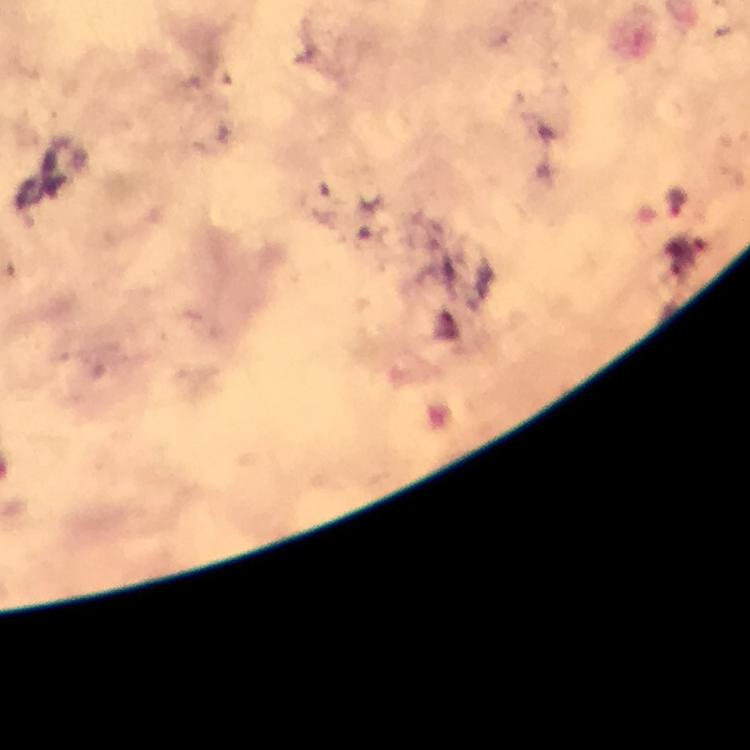
malaria_parasite_locations: 'approximate centers as [x, y] in pixels: [677, 199]'
stain: Giemsa
image_size: 750×750 pixels
magnification: 100x
capture: smartphone mounted on the microscope
preparation: thick blood film
immersion_oil: applied
context: from a malaria diagnostic workup
cropped_from: a single field of view